Locate every Plasmodium ovale-infected red blood cell.
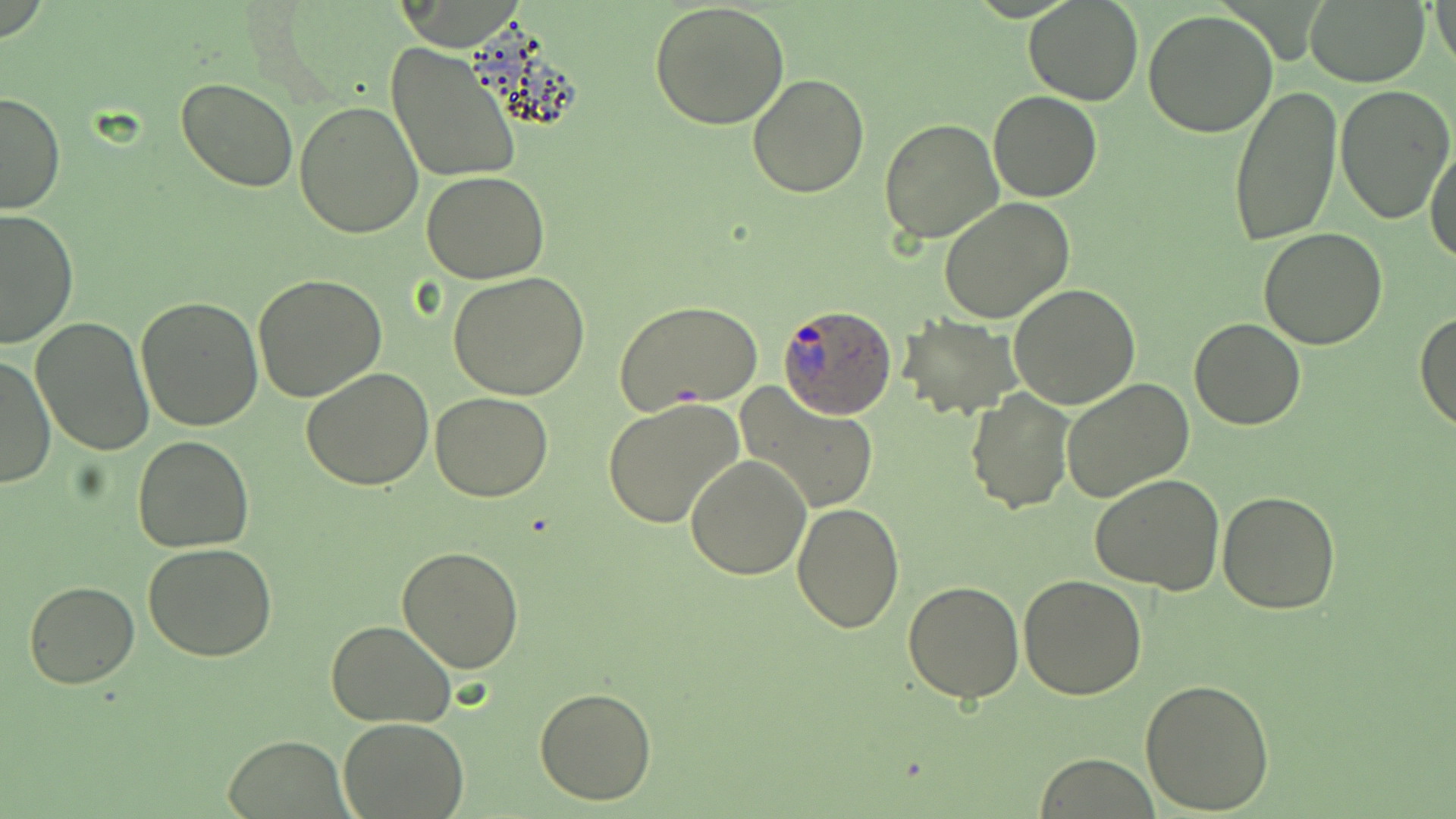

Approximate bounding boxes as (x1, y1, x2, y2) in pixels.
Plasmodium ovale-infected red blood cells: (775, 302, 899, 420).

Summary:
  - Uninfected red blood cell locations: (1024, 0, 1144, 107), (1305, 0, 1431, 86), (1431, 0, 1456, 72), (648, 3, 790, 132), (1143, 10, 1279, 138), (386, 41, 521, 183), (748, 72, 870, 196), (176, 76, 299, 194), (1333, 82, 1454, 224), (1228, 84, 1341, 246), (0, 89, 66, 214), (989, 90, 1103, 203), (294, 99, 424, 239), (878, 118, 1003, 246), (1425, 141, 1456, 264), (421, 171, 549, 283), (939, 196, 1074, 324), (1, 208, 77, 349), (1260, 227, 1386, 349), (447, 271, 591, 399), (252, 274, 387, 402), (1009, 284, 1141, 409), (136, 295, 265, 431), (614, 299, 764, 413), (1415, 309, 1456, 432), (896, 315, 1021, 420), (30, 316, 158, 455), (1190, 319, 1306, 432), (1, 354, 54, 487), (302, 367, 433, 491), (1061, 377, 1193, 503), (737, 384, 881, 515), (965, 387, 1075, 514), (430, 392, 553, 500), (603, 398, 745, 528), (132, 434, 254, 553), (684, 455, 812, 580), (1089, 472, 1225, 593), (1216, 490, 1343, 613), (791, 502, 903, 632), (142, 543, 278, 661), (396, 545, 524, 674), (1018, 574, 1150, 699), (24, 580, 139, 689), (903, 580, 1026, 703), (326, 618, 457, 729), (1140, 678, 1275, 814), (534, 686, 656, 805), (338, 717, 470, 819), (223, 736, 349, 816), (1035, 753, 1158, 818)
  - Slide-level diagnosis: Plasmodium ovale
  - Modality: optical microscopy
  - Preparation: thin blood smear
  - Magnification: 1000x
  - Image size: 1456×819 pixels
  - Field of view: one of a larger specimen
  - Stain: May-Grünwald-Giemsa